Classify the preparation.
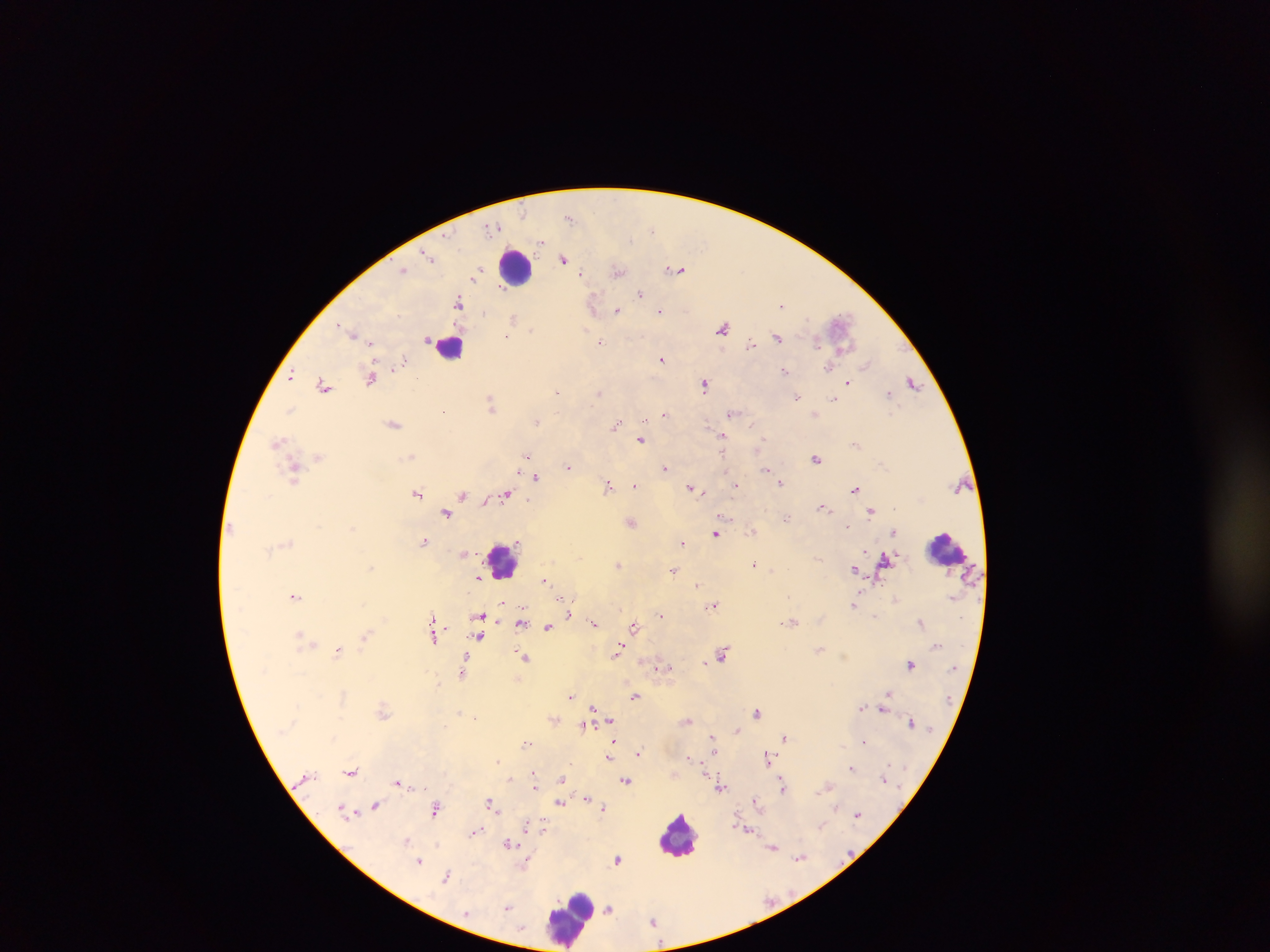
This is a thick smear.

capture = mobile-phone photograph through a microscope
country = Ghana
Plasmodium parasite locations = approximate centers as {x, y} in pixels: {569, 217}, {493, 227}, {652, 229}, {541, 242}, {426, 253}, {430, 257}, {563, 259}, {676, 269}, {403, 270}, {617, 271}, {581, 273}, {474, 275}, {501, 287}, {640, 294}, {593, 301}, {459, 302}, {781, 305}, {617, 310}, {660, 311}, {513, 318}, {839, 320}, {339, 326}, {723, 327}, {344, 328}, {531, 330}, {586, 330}, {351, 333}, {506, 337}, {777, 337}, {428, 339}, {372, 342}, {600, 342}, {818, 343}, {751, 345}, {842, 348}, {661, 359}, {404, 361}, {866, 364}, {827, 368}, {785, 370}, {292, 376}, {371, 378}, {913, 382}, {704, 383}, {849, 383}, {324, 384}, {557, 391}, {598, 393}, {889, 393}, {797, 397}, {834, 400}, {491, 404}, {290, 409}, {443, 411}, {664, 413}, {731, 414}, {645, 419}, {537, 422}, {394, 424}, {616, 425}, {708, 425}, {751, 425}, {723, 436}, {641, 439}, {763, 439}, {279, 442}, {855, 444}, {723, 453}, {527, 454}, {318, 456}, {411, 456}, {816, 459}, {568, 466}, {665, 468}, {767, 469}, {295, 472}, {518, 473}, {536, 477}, {781, 483}, {607, 485}, {634, 485}, {736, 485}, {691, 488}, {855, 489}, {418, 493}, {704, 493}, {505, 494}, {462, 495}, {485, 501}, {822, 506}, {872, 512}, {446, 513}, {725, 517}, {786, 518}, {631, 522}, {848, 525}, {751, 531}, {893, 532}, {715, 534}, {424, 542}, {682, 542}, {865, 550}, {885, 558}, {755, 563}, {618, 564}, {372, 567}, {673, 569}, {855, 570}, {478, 577}, {544, 580}, {879, 583}, {697, 585}, {295, 596}, {787, 597}, {564, 598}, {896, 599}, {503, 603}, {714, 604}, {854, 605}, {569, 613}, {661, 615}, {478, 616}, {432, 617}, {521, 622}, {793, 622}, {921, 622}, {594, 623}, {548, 626}, {634, 626}, {299, 634}, {435, 636}, {479, 636}, {365, 637}, {820, 649}, {338, 651}, {617, 652}, {723, 652}, {524, 656}, {705, 662}, {911, 664}, {658, 668}, {461, 672}, {888, 693}, {571, 696}, {635, 696}, {861, 707}, {593, 708}, {882, 709}, {383, 711}, {459, 712}, {757, 712}, {475, 717}, {610, 720}, {688, 721}, {911, 722}, {584, 727}, {737, 730}, {711, 735}, {785, 737}, {614, 740}, {863, 741}, {527, 743}, {714, 752}, {638, 753}, {689, 756}, {609, 757}, {768, 758}, {499, 761}, {851, 768}, {351, 771}, {534, 772}, {705, 775}, {509, 779}, {561, 779}, {884, 779}, {626, 781}, {398, 782}, {535, 787}, {783, 787}, {721, 788}, {587, 797}, {591, 800}, {755, 800}, {491, 803}, {560, 803}, {375, 806}, {603, 807}, {435, 808}, {342, 810}, {348, 812}, {857, 814}, {528, 825}, {821, 825}, {542, 826}, {748, 830}, {476, 831}, {406, 840}, {509, 844}, {773, 847}, {799, 858}, {618, 859}, {419, 861}, {527, 863}, {446, 877}, {508, 907}, {609, 908}
field of view = single
image size = 1270×952 pixels
leukocyte locations = approximate centers as {x, y} in pixels: {516, 267}, {451, 345}, {946, 549}, {504, 558}, {679, 834}, {570, 918}